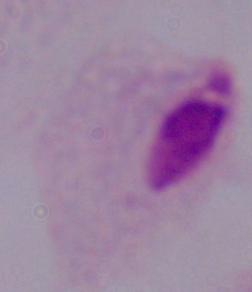

magnification: 1000x
identification: trichomonad
modality: photomicrograph